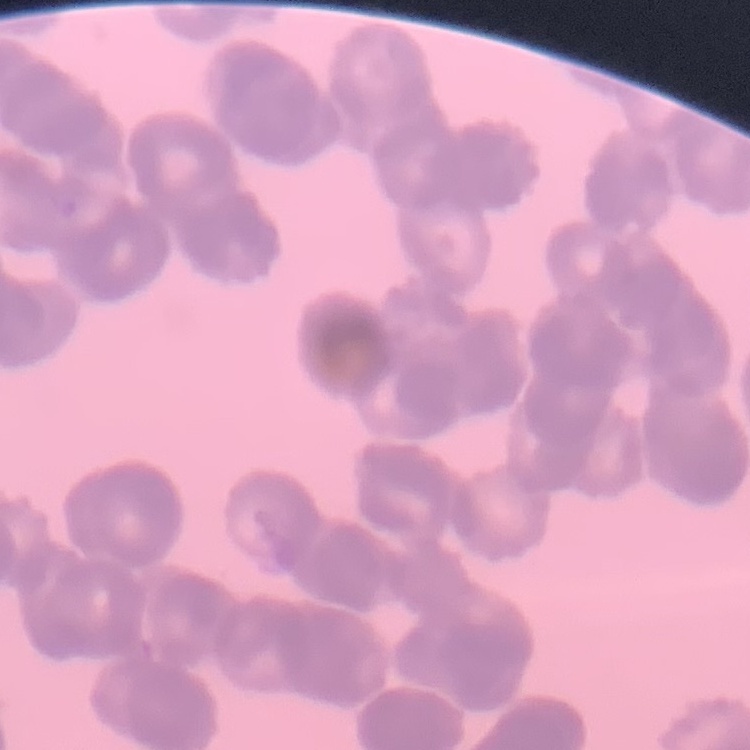 The red blood cells show rouleaux formation. Field's or Giemsa stain. Thin blood smear. Square crop of a larger photomicrograph.